Classify this cell by malaria status.
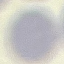

It is uninfected.

Summary:
  - Preparation: thin smear
  - Stain: Giemsa
  - Image type: automatically extracted cell patch, resized to 64 × 64 pixels
  - Capture: smartphone through the microscope eyepiece